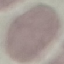

result = no malaria parasites detected
image type = cell patch, automatically extracted from a larger field of view and resized to 64 × 64 pixels
capture = smartphone through the microscope eyepiece
preparation = thin blood film
stain = Giemsa